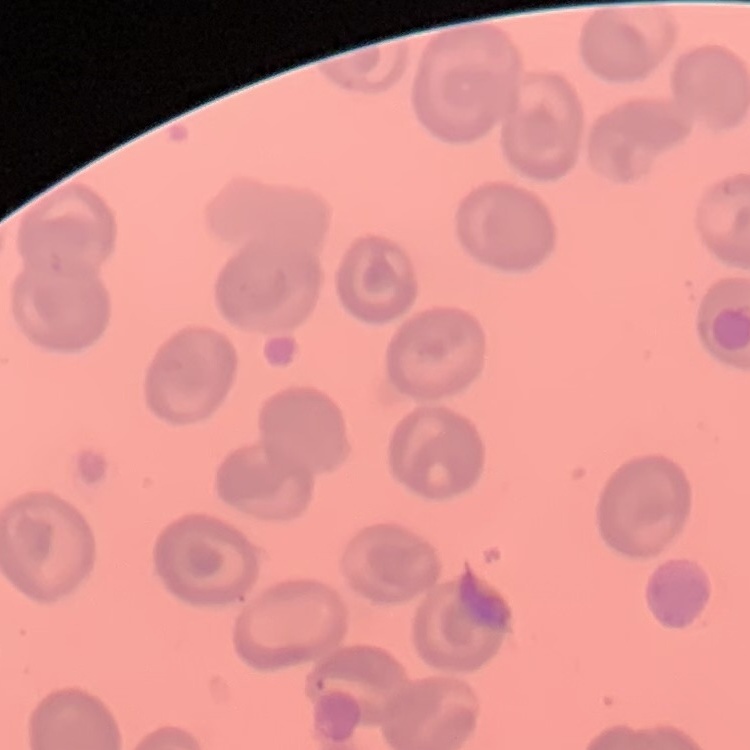
Summary:
  - Red blood cell morphology: no rouleaux formation
  - Stain: Field's or Giemsa
  - Preparation: thin blood film
  - Image type: square crop of a larger photomicrograph